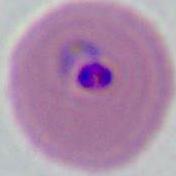
Summary:
  - Identification: Plasmodium
  - Modality: photomicrograph
  - Magnification: 400x or 1000x